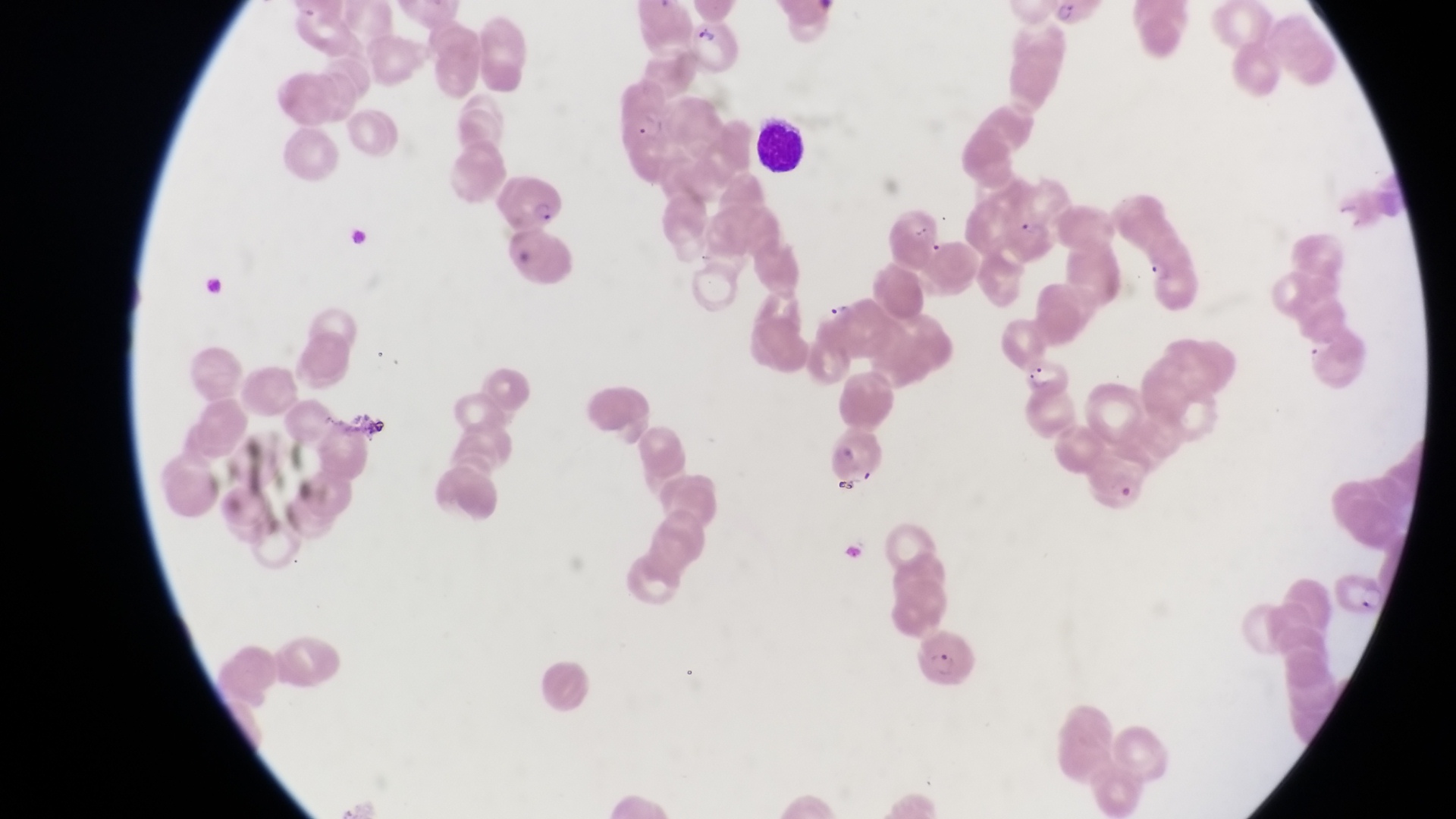
Approximate bounding boxes as [left, top, right, bottom] in pixels.
Summary:
  - Parasitised red blood cell locations: [492, 172, 564, 233], [1015, 356, 1070, 399], [1084, 455, 1150, 516], [1331, 571, 1387, 618], [918, 632, 982, 690]
  - Artifact (platelet-like body, stain precipitate, or debris) locations: [908, 221, 935, 242], [510, 241, 546, 265], [351, 413, 391, 446], [832, 479, 865, 495]
  - Trophozoite locations: [1136, 253, 1170, 285], [821, 298, 851, 321]
  - Preparation: thin blood smear
  - Field of view: single
  - Magnification: 1000x
  - Capture: smartphone photograph through the eyepiece of an Olympus CX-23 microscope
  - Image size: 1456×819 pixels
  - Country: Uganda